Identify the preparation type.
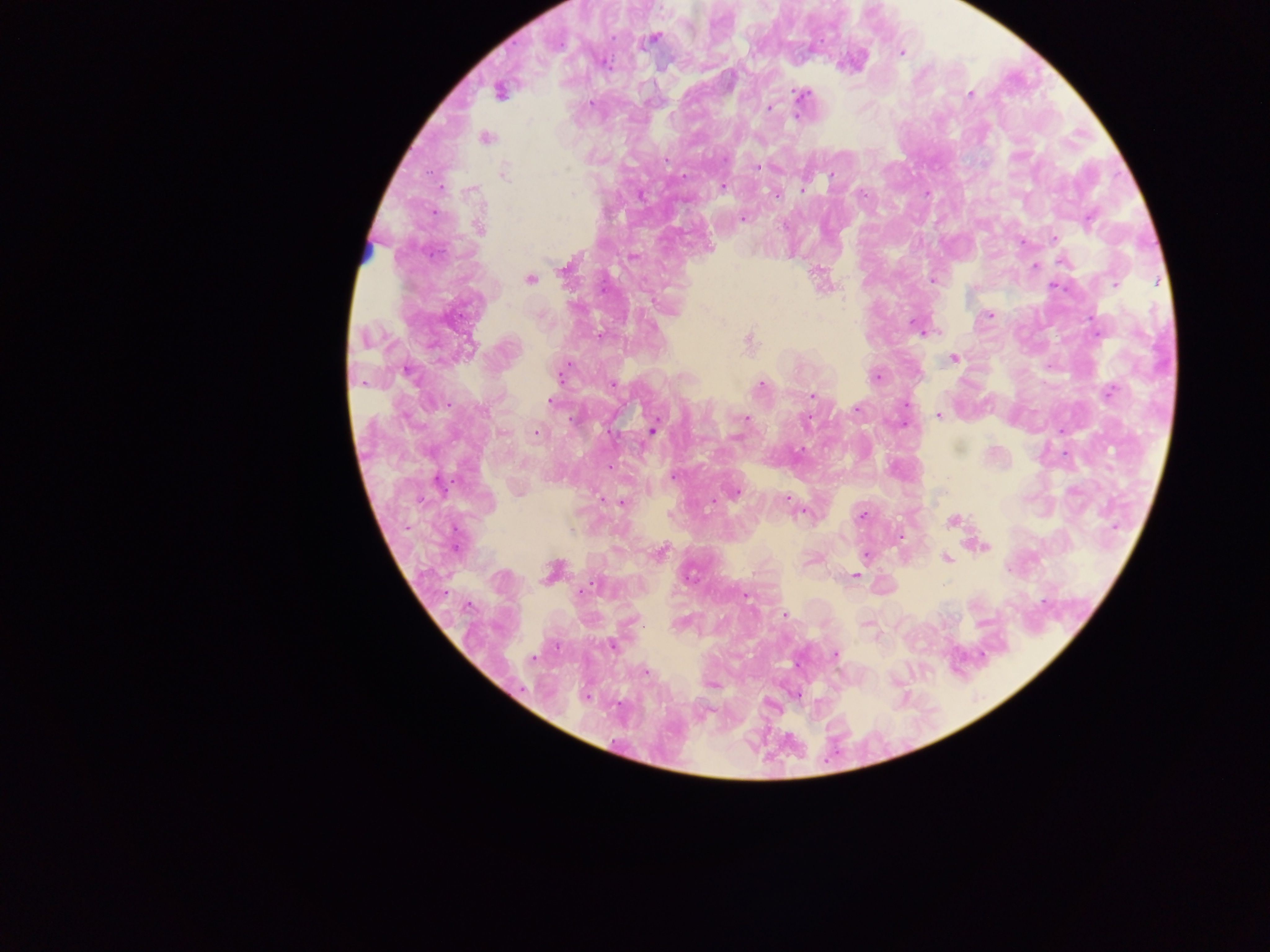

This is a thick smear.

Approximate centers as [x, y] in pixels. Plasmodium parasite locations: [653, 38], [901, 53], [500, 92], [970, 93], [802, 94], [590, 103], [769, 109], [486, 138], [724, 159], [666, 160], [757, 167], [504, 174], [832, 175], [723, 187], [802, 190], [862, 193], [776, 195], [744, 219], [1089, 220], [480, 228], [1055, 238], [1022, 242], [1064, 262], [1035, 266], [564, 268], [530, 279], [932, 280], [1115, 284], [1054, 287], [990, 315], [916, 328], [748, 340], [954, 358], [562, 372], [876, 378], [613, 385], [761, 385], [1110, 392], [812, 395], [551, 401], [857, 408], [939, 416], [574, 419], [746, 419], [806, 422], [654, 429], [538, 433], [737, 436], [673, 476], [439, 483], [735, 493], [786, 499], [619, 501], [792, 503], [802, 512], [862, 515], [953, 520], [982, 546], [660, 553], [866, 554], [946, 558], [552, 572], [855, 576], [590, 588], [583, 590], [746, 596], [784, 615], [613, 646], [835, 655], [533, 658], [645, 672]. Single field of view. Mobile-phone photograph taken through the microscope. Image is 1270×952 pixels. Collected in Ghana.